State which parasite is depicted.
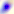
This is Toxoplasma gondii.

Summary:
  - Magnification: 400x
  - Modality: micrograph